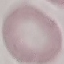

malaria status = uninfected
preparation = thin blood film
image type = cell patch, automatically extracted from a larger field of view and resized to 64 × 64 pixels
stain = Giemsa
capture = smartphone through the microscope eyepiece